Locate every Plasmodium falciparum-infected red blood cell.
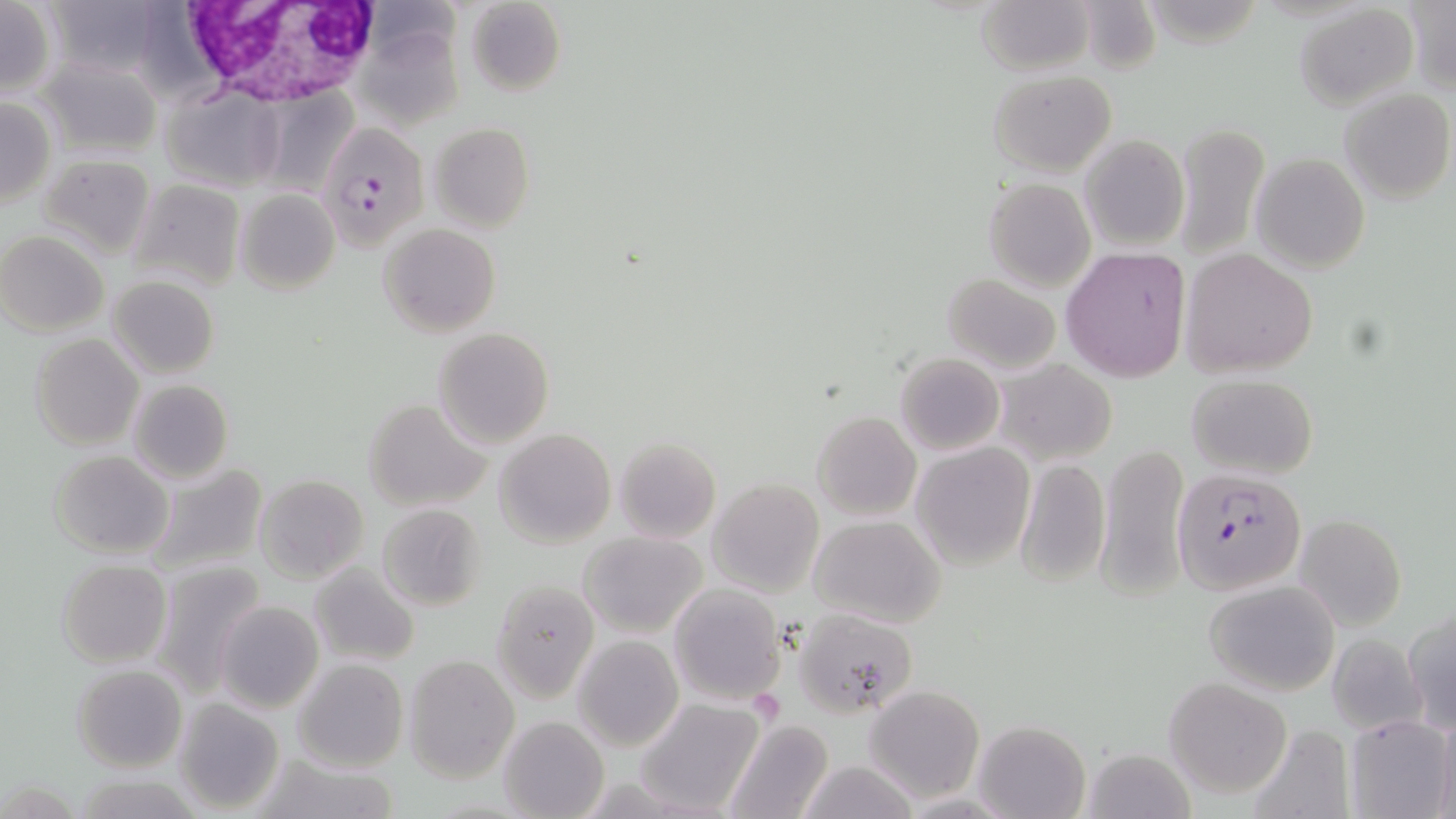

Approximate bounding boxes as (x1, y1, x2, y2) in pixels.
Plasmodium falciparum-infected red blood cells: (314, 122, 433, 264), (1174, 466, 1307, 597).

Summary:
  - Uninfected red blood cell locations: (41, 0, 176, 83), (465, 0, 567, 97), (976, 0, 1095, 75), (0, 1, 55, 101), (1407, 2, 1456, 95), (1294, 3, 1418, 112), (355, 9, 466, 128), (38, 58, 161, 157), (988, 68, 1116, 178), (160, 86, 288, 193), (1340, 87, 1455, 204), (0, 97, 54, 207), (428, 122, 536, 234), (1172, 123, 1269, 261), (1080, 135, 1190, 251), (1251, 152, 1371, 274), (37, 154, 155, 258), (983, 177, 1097, 292), (127, 179, 247, 292), (1021, 183, 1157, 339), (234, 188, 341, 295), (379, 222, 502, 337), (1, 230, 109, 336), (1060, 246, 1191, 382), (1179, 247, 1318, 379), (942, 273, 1062, 374), (106, 275, 219, 379), (432, 328, 554, 448), (29, 333, 144, 452), (896, 352, 1005, 455), (995, 360, 1115, 464), (1186, 373, 1317, 478), (127, 379, 233, 485), (361, 398, 490, 511), (811, 411, 921, 521), (494, 428, 616, 548), (614, 436, 721, 543), (1097, 440, 1189, 601), (910, 442, 1035, 571), (51, 450, 172, 561), (1013, 459, 1111, 588), (146, 464, 271, 580), (254, 474, 369, 586), (708, 478, 825, 598), (376, 504, 486, 612), (807, 514, 947, 627), (1295, 514, 1406, 633), (579, 531, 707, 639), (58, 559, 170, 667), (150, 559, 269, 698), (309, 562, 421, 668), (492, 578, 599, 702), (1203, 580, 1341, 696), (668, 584, 786, 707), (215, 601, 323, 715), (1403, 606, 1456, 733), (794, 608, 921, 717), (1327, 633, 1430, 735), (574, 634, 683, 751), (402, 654, 518, 782), (293, 658, 408, 772), (72, 665, 187, 772), (1164, 675, 1293, 796), (864, 684, 984, 802), (173, 697, 285, 815), (634, 698, 766, 818), (498, 715, 609, 818), (1344, 715, 1453, 819), (721, 719, 834, 819), (973, 720, 1089, 819), (1245, 723, 1355, 819), (1082, 746, 1197, 819), (249, 751, 395, 819), (794, 759, 918, 819), (71, 772, 202, 818)
  - Platelet locations: (748, 689, 786, 727)
  - White blood cell locations: (167, 0, 392, 107)
  - Slide-level diagnosis: Plasmodium falciparum
  - Preparation: thin blood film
  - Magnification: 1000x
  - Modality: light microscopy
  - Stain: May-Grünwald-Giemsa
  - Field of view: one of a larger specimen
  - Image size: 1456×819 pixels